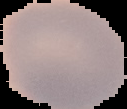
image_size: 127×109 pixels
image_type: segmented cell region with the area outside set to black
preparation: thin blood smear
result: negative for malaria parasites